Comment on the morphology of the red blood cells.
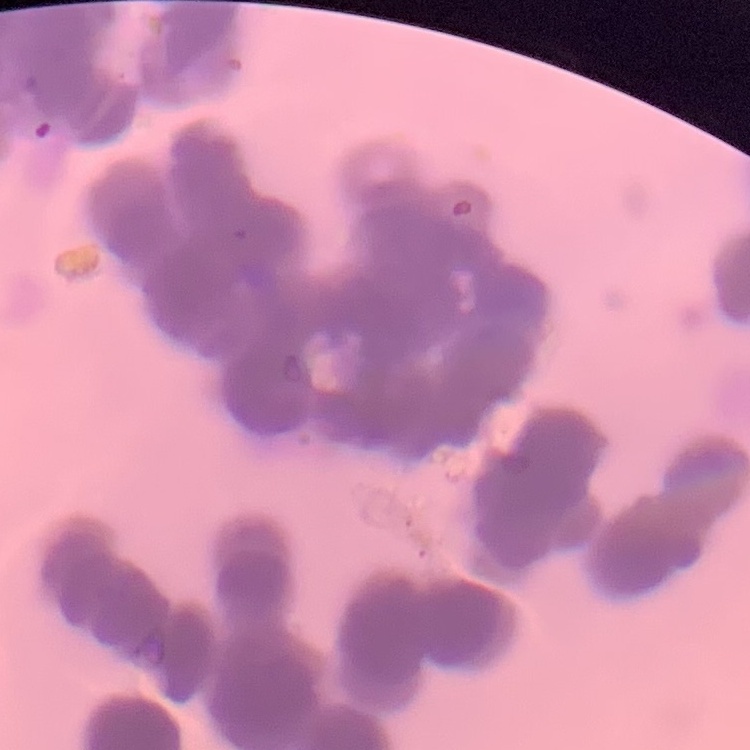
Rouleaux formation.

{
  "preparation": "thin peripheral smear",
  "image_type": "one tile cut from a larger photomicrograph",
  "stain": "Field's or Giemsa"
}